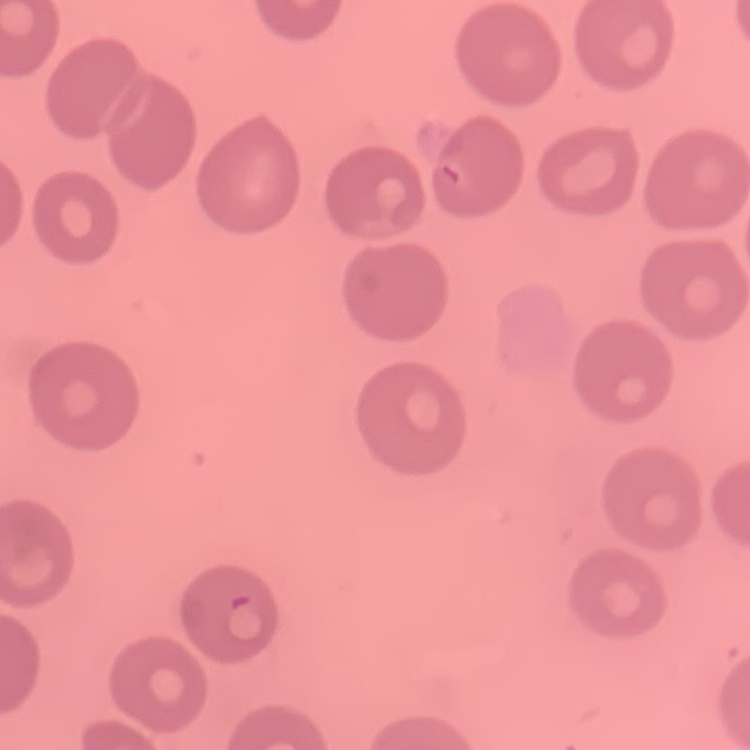
Summary:
  - Red blood cell morphology: no rouleaux formation
  - Preparation: thin blood smear
  - Stain: Field's or Giemsa
  - Image type: square crop of a larger photomicrograph